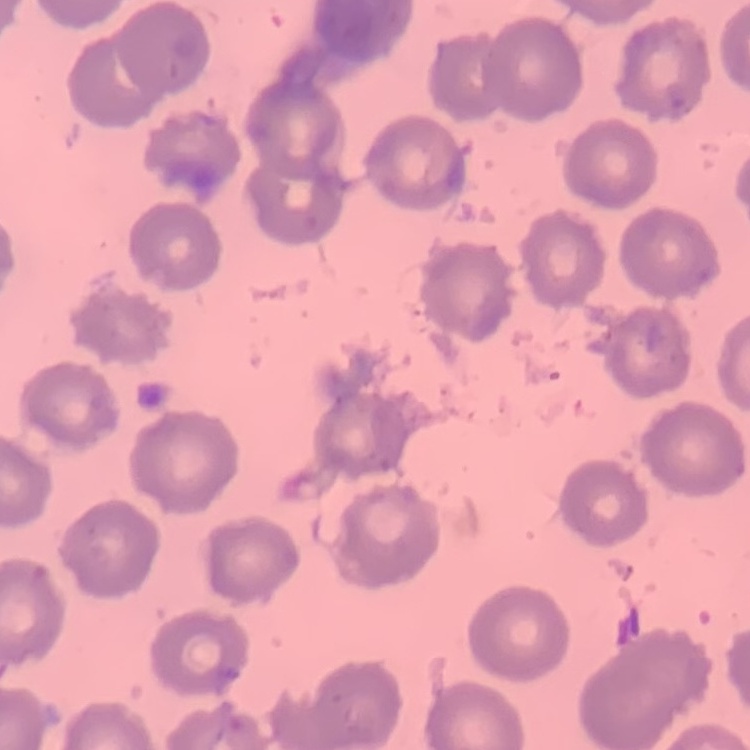

Summary:
  - Red blood cell morphology: no rouleaux formation
  - Preparation: thin blood film
  - Stain: Field's or Giemsa
  - Image type: square crop of a larger photomicrograph